Assess the morphology of the erythrocytes.
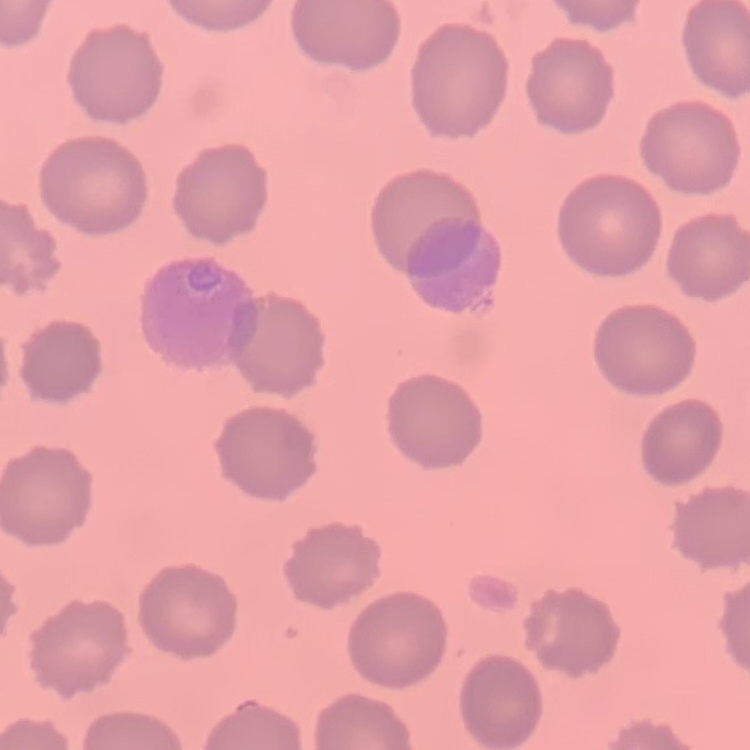

They show no rouleaux formation.

{
  "stain": "Field's or Giemsa",
  "image_type": "one tile cut from a larger photomicrograph",
  "preparation": "thin peripheral smear"
}